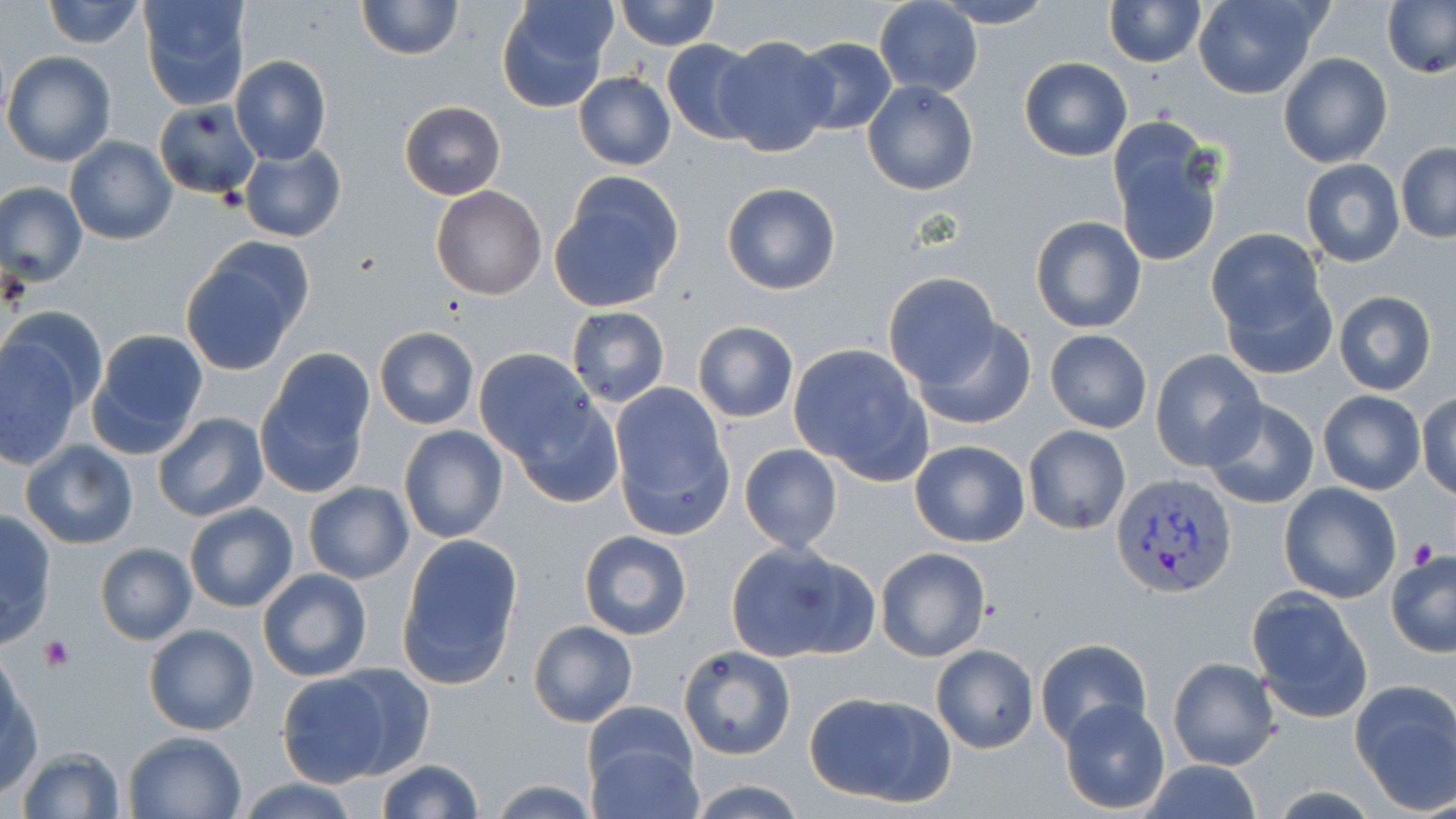

Approximate bounding boxes as named x1/y1/x2/y2 corners in pixels. Platelet locations: (x1=1410, y1=535, x2=1439, y2=568), (x1=39, y1=635, x2=75, y2=672). Plasmodium vivax-infected red blood cell locations: (x1=1111, y1=474, x2=1237, y2=596). Uninfected red blood cell locations: (x1=41, y1=0, x2=145, y2=49), (x1=137, y1=0, x2=253, y2=110), (x1=355, y1=0, x2=463, y2=61), (x1=494, y1=0, x2=616, y2=112), (x1=614, y1=0, x2=720, y2=51), (x1=1193, y1=0, x2=1324, y2=100), (x1=874, y1=1, x2=982, y2=97), (x1=932, y1=1, x2=1053, y2=28), (x1=1101, y1=1, x2=1205, y2=66), (x1=1382, y1=1, x2=1456, y2=78), (x1=714, y1=35, x2=837, y2=157), (x1=792, y1=36, x2=898, y2=136), (x1=661, y1=39, x2=762, y2=144), (x1=2, y1=51, x2=117, y2=166), (x1=1278, y1=53, x2=1392, y2=168), (x1=230, y1=55, x2=332, y2=166), (x1=1019, y1=56, x2=1133, y2=162), (x1=574, y1=72, x2=675, y2=171), (x1=862, y1=81, x2=979, y2=196), (x1=153, y1=100, x2=263, y2=201), (x1=399, y1=101, x2=506, y2=199), (x1=1104, y1=115, x2=1226, y2=267), (x1=65, y1=136, x2=177, y2=245), (x1=1395, y1=143, x2=1456, y2=243), (x1=238, y1=144, x2=346, y2=243), (x1=1300, y1=159, x2=1404, y2=268), (x1=550, y1=174, x2=685, y2=312), (x1=0, y1=181, x2=88, y2=287), (x1=721, y1=182, x2=842, y2=295), (x1=429, y1=185, x2=546, y2=300), (x1=1029, y1=215, x2=1147, y2=335), (x1=1208, y1=229, x2=1335, y2=374), (x1=179, y1=247, x2=311, y2=375), (x1=882, y1=272, x2=999, y2=387), (x1=1333, y1=290, x2=1438, y2=395), (x1=4, y1=306, x2=105, y2=410), (x1=566, y1=307, x2=669, y2=406), (x1=912, y1=319, x2=1037, y2=429), (x1=692, y1=322, x2=798, y2=422), (x1=373, y1=326, x2=479, y2=430), (x1=86, y1=328, x2=209, y2=459), (x1=1044, y1=328, x2=1153, y2=433), (x1=0, y1=338, x2=83, y2=470), (x1=370, y1=339, x2=589, y2=445), (x1=788, y1=343, x2=933, y2=484), (x1=258, y1=348, x2=374, y2=490), (x1=474, y1=349, x2=601, y2=465), (x1=1150, y1=349, x2=1266, y2=469), (x1=608, y1=383, x2=734, y2=538), (x1=1317, y1=391, x2=1426, y2=494), (x1=1416, y1=393, x2=1455, y2=502), (x1=1199, y1=398, x2=1321, y2=512), (x1=513, y1=401, x2=626, y2=507), (x1=153, y1=413, x2=269, y2=524), (x1=399, y1=425, x2=508, y2=543), (x1=1022, y1=425, x2=1130, y2=535), (x1=1250, y1=428, x2=1379, y2=568), (x1=908, y1=439, x2=1030, y2=548), (x1=20, y1=440, x2=138, y2=550), (x1=739, y1=443, x2=841, y2=553), (x1=303, y1=481, x2=413, y2=584), (x1=1278, y1=483, x2=1403, y2=604), (x1=184, y1=503, x2=299, y2=612), (x1=0, y1=509, x2=57, y2=647), (x1=578, y1=530, x2=694, y2=640), (x1=398, y1=534, x2=523, y2=690), (x1=724, y1=541, x2=875, y2=664), (x1=95, y1=543, x2=196, y2=646), (x1=874, y1=547, x2=993, y2=663), (x1=1386, y1=549, x2=1456, y2=657), (x1=257, y1=567, x2=373, y2=683), (x1=1247, y1=589, x2=1374, y2=723), (x1=528, y1=619, x2=638, y2=729), (x1=144, y1=623, x2=259, y2=735), (x1=1036, y1=638, x2=1151, y2=747), (x1=679, y1=644, x2=796, y2=760), (x1=931, y1=645, x2=1037, y2=752), (x1=1167, y1=656, x2=1281, y2=771), (x1=328, y1=662, x2=437, y2=778), (x1=274, y1=672, x2=396, y2=789), (x1=1, y1=676, x2=43, y2=798), (x1=1350, y1=682, x2=1456, y2=812), (x1=802, y1=689, x2=956, y2=810), (x1=1059, y1=699, x2=1170, y2=815), (x1=124, y1=731, x2=246, y2=818), (x1=585, y1=738, x2=703, y2=818), (x1=15, y1=747, x2=126, y2=819), (x1=377, y1=759, x2=484, y2=818), (x1=1141, y1=761, x2=1264, y2=819), (x1=488, y1=777, x2=598, y2=816), (x1=237, y1=779, x2=361, y2=818), (x1=685, y1=779, x2=807, y2=818). Slide-level diagnosis: Plasmodium vivax. May-Grünwald-Giemsa stain. Image is 1456×819 pixels. Single field of view. Thin blood film. Light microscopy. 1000x magnification.